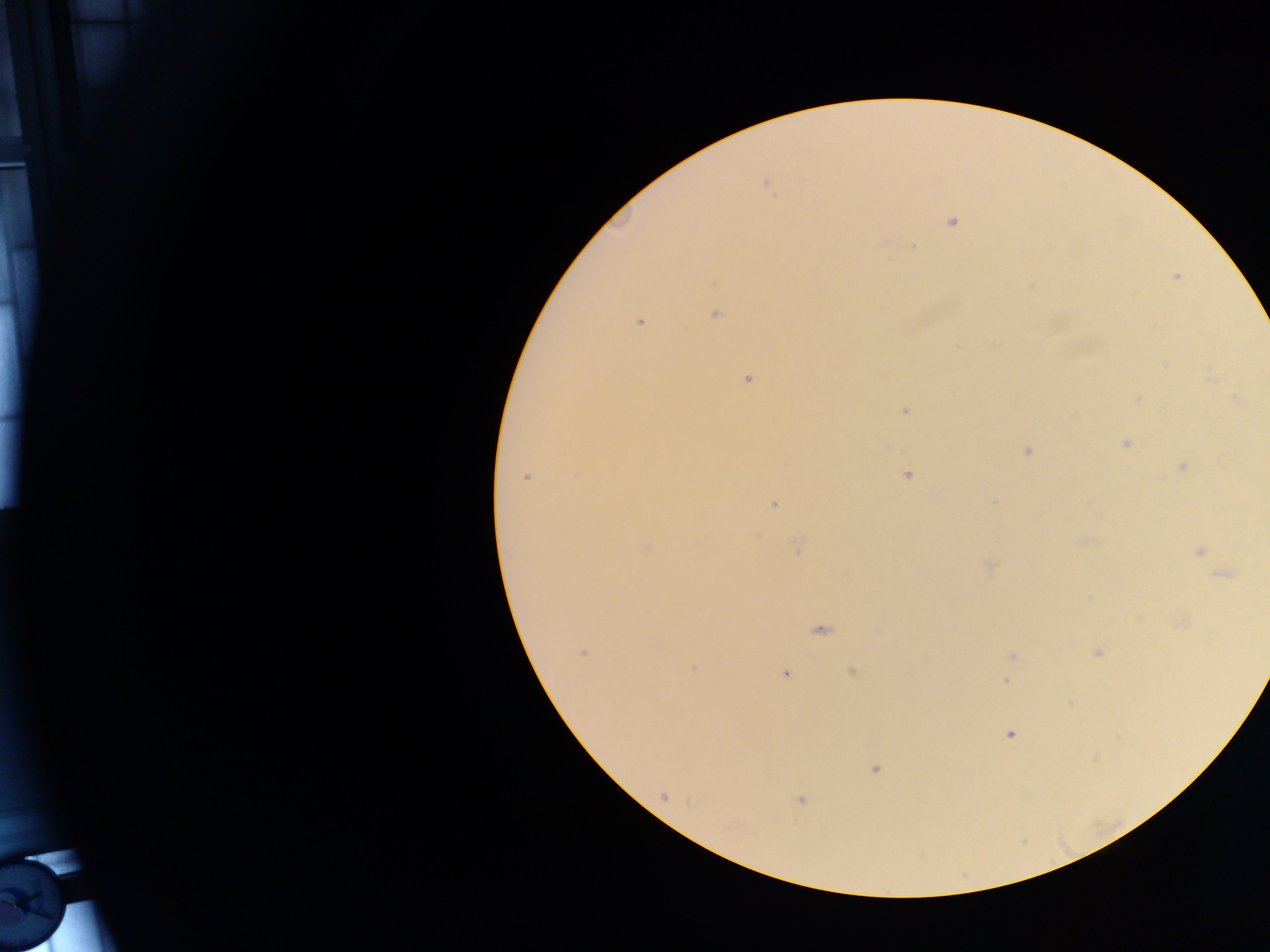
Approximate centers as (x, y) in pixels.
Summary:
  - Malaria parasite locations: (765, 183), (952, 223), (914, 246), (1176, 277), (715, 314), (639, 322), (1211, 378), (748, 381), (1138, 398), (1236, 400), (906, 412), (1125, 445), (1026, 451), (1182, 466), (907, 475), (526, 477), (994, 501), (773, 504), (757, 535), (1083, 541), (797, 548), (645, 550), (1200, 551), (991, 565), (1226, 575), (820, 630), (582, 652), (1097, 652), (1012, 655), (693, 667), (852, 672), (786, 674), (1005, 681), (1010, 735), (875, 770), (663, 795), (800, 800)
  - Image size: 1270×952 pixels
  - Country: Ghana
  - Field of view: single
  - Preparation: thick blood smear
  - Capture: mobile-phone photograph through a microscope